Comment on the morphology of the erythrocytes.
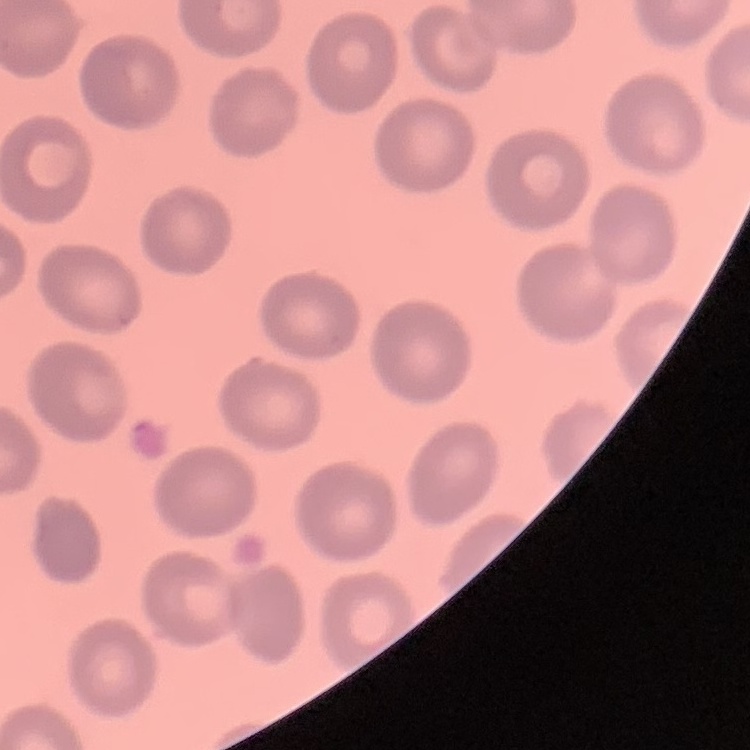

No rouleaux formation.

image type = one tile cut from a larger photomicrograph
preparation = thin blood film
stain = Field's or Giemsa